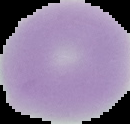

image_type: segmented cell region on a black background
malaria_status: uninfected
preparation: thin blood smear
image_size: 130×124 pixels